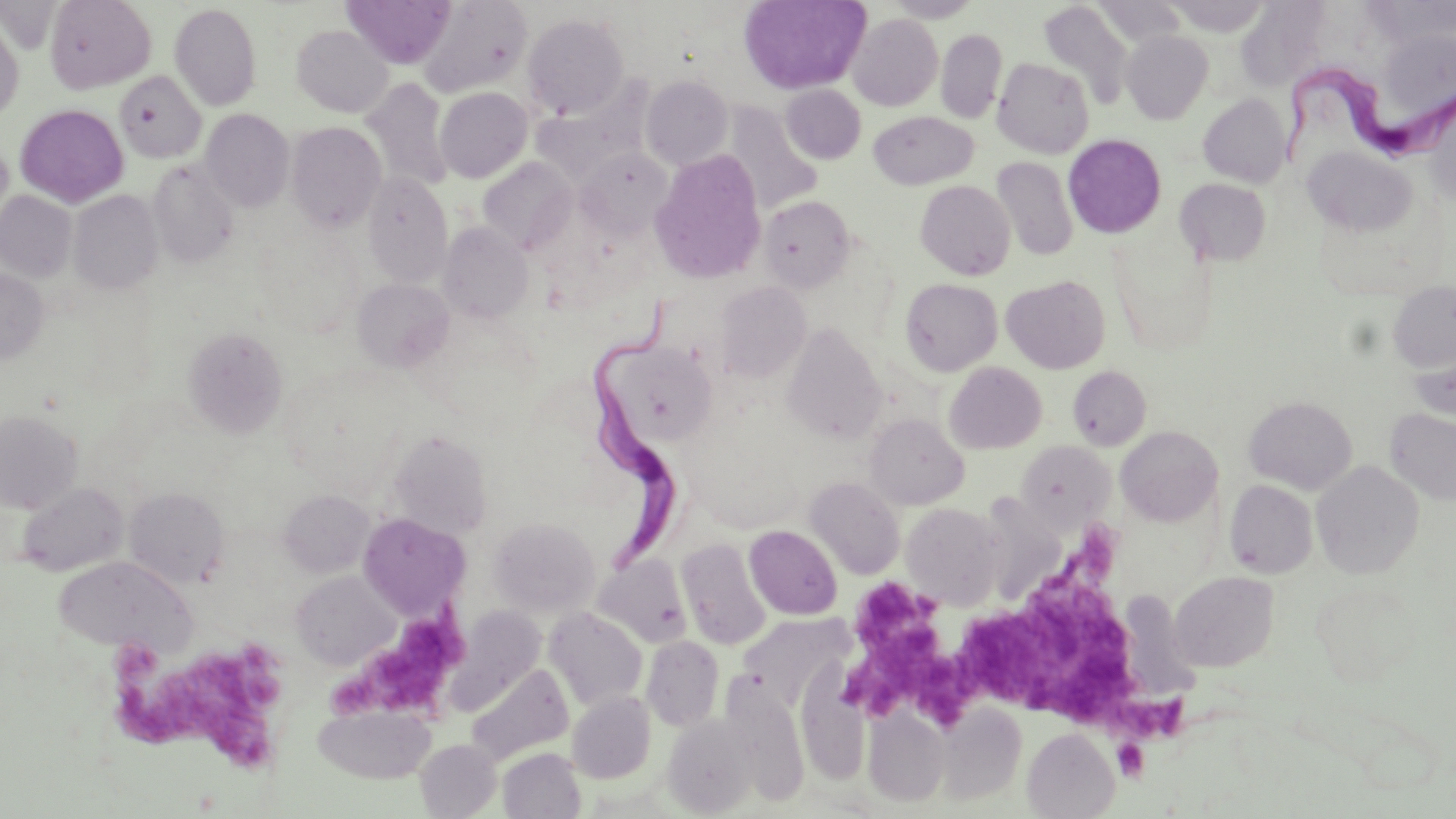

slide-level diagnosis = Trypanosoma brucei
modality = light microscopy
uninfected red blood cell locations = approximate bounding boxes as (x1,y1)-(x2,y2) corner pairs in pixels: (45,0)-(156,93), (342,0)-(457,69), (418,0)-(532,97), (739,0)-(870,94), (884,0)-(983,22), (1240,0)-(1329,88), (1037,2)-(1135,109), (1092,2)-(1187,47), (169,3)-(262,111), (522,12)-(630,119), (847,13)-(943,111), (0,14)-(24,123), (291,25)-(393,117), (936,28)-(1007,123), (1122,30)-(1213,123), (992,57)-(1094,159), (114,71)-(207,163), (640,74)-(734,170), (362,77)-(453,192), (781,85)-(866,164), (435,87)-(532,182), (1198,93)-(1290,187), (723,103)-(823,214), (14,104)-(129,207), (200,109)-(294,212), (868,111)-(977,189), (286,122)-(386,232), (1063,134)-(1167,238), (0,137)-(13,229), (1301,147)-(1419,238), (577,148)-(674,239), (649,151)-(767,284), (992,156)-(1078,261), (478,157)-(577,254), (148,160)-(239,269), (362,173)-(453,287), (1175,178)-(1271,265), (915,180)-(1016,280), (70,189)-(162,295), (0,191)-(77,282), (760,196)-(855,292), (438,222)-(532,323), (0,268)-(49,364), (1001,274)-(1110,373), (352,278)-(455,372), (900,278)-(1003,376), (714,281)-(810,383), (1387,282)-(1456,373), (781,323)-(886,443), (183,326)-(288,439), (602,339)-(719,446), (1407,348)-(1455,424), (944,362)-(1047,454), (1067,365)-(1151,450), (1244,396)-(1357,494), (1384,408)-(1456,507), (0,410)-(82,512), (865,413)-(968,509), (1115,426)-(1223,526), (386,428)-(493,540), (1016,441)-(1114,532), (1312,460)-(1424,580), (804,476)-(905,579), (1225,480)-(1318,578), (16,482)-(129,576), (124,487)-(229,587), (278,490)-(374,577), (991,490)-(1070,612), (902,502)-(1004,609), (358,513)-(469,618), (489,517)-(600,616), (745,525)-(842,619), (677,538)-(771,651), (593,554)-(692,648), (53,556)-(196,656), (291,571)-(398,669), (1170,571)-(1279,672), (1126,589)-(1207,706), (544,607)-(648,710), (740,614)-(851,707), (641,636)-(724,731), (466,665)-(574,765), (567,692)-(656,783), (313,703)-(436,783), (935,705)-(1027,803), (863,708)-(950,806), (662,715)-(758,816), (1023,728)-(1119,818), (415,739)-(502,818), (498,748)-(586,819)
Trypanosoma brucei locations = approximate bounding boxes as (x1,y1)-(x2,y2) corner pairs in pixels: (1278,69)-(1455,170), (584,291)-(690,573)
stain = May-Grünwald-Giemsa
preparation = thin blood smear
image size = 1456×819 pixels
platelet locations = approximate bounding boxes as (x1,y1)-(x2,y2) corner pairs in pixels: (983,529)-(1192,746), (847,576)-(972,725), (330,604)-(475,719), (110,645)-(283,780), (1112,739)-(1149,782)
field of view = one of a larger specimen
magnification = 1000x